Identify the blood parasite species.
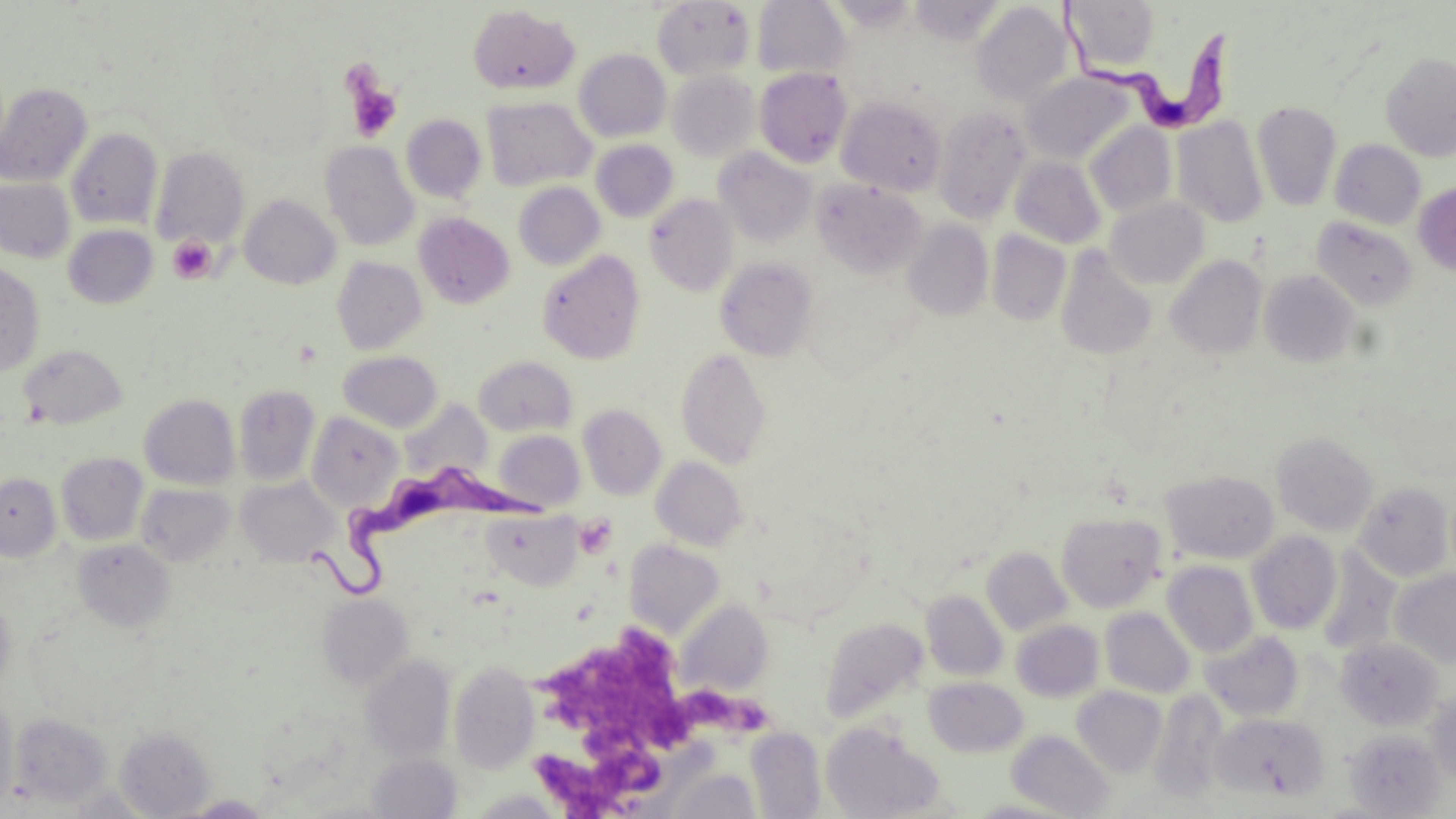
Trypanosoma brucei.

{
  "stain": "May-Grünwald-Giemsa",
  "field_of_view": "one of a larger specimen",
  "preparation": "thin blood film",
  "uninfected_red_blood_cell_locations": "approximate bounding boxes as (x1, y1, x2, y2) in pixels: (753, 0, 852, 78), (1064, 1, 1163, 76), (652, 2, 755, 79), (971, 2, 1072, 106), (467, 5, 580, 96), (574, 49, 671, 142), (1381, 52, 1456, 161), (754, 68, 852, 167), (667, 69, 760, 161), (1021, 71, 1137, 163), (0, 82, 92, 187), (482, 96, 595, 191), (837, 96, 947, 196), (1253, 100, 1341, 211), (933, 105, 1032, 222), (401, 115, 486, 203), (1172, 117, 1268, 227), (1085, 122, 1177, 217), (66, 127, 162, 229), (1330, 139, 1426, 229), (320, 140, 419, 252), (591, 140, 678, 222), (150, 146, 250, 248), (714, 147, 817, 247), (1010, 156, 1105, 248), (0, 177, 74, 263), (811, 179, 928, 279), (1413, 181, 1456, 275), (513, 182, 605, 269), (240, 194, 340, 289), (645, 194, 739, 296), (1105, 197, 1209, 289), (413, 212, 514, 308), (1312, 216, 1418, 312), (903, 220, 993, 321), (63, 225, 158, 308), (986, 231, 1070, 326), (1054, 246, 1158, 361), (538, 250, 646, 364), (1166, 255, 1267, 360), (332, 256, 428, 354), (715, 258, 818, 360), (0, 264, 46, 377), (1259, 269, 1361, 368), (19, 344, 127, 429), (676, 347, 772, 468), (337, 351, 443, 432), (473, 355, 577, 436), (235, 385, 320, 486), (139, 395, 240, 490), (398, 400, 493, 483), (578, 403, 667, 500), (306, 411, 405, 511), (493, 429, 585, 511), (1272, 431, 1378, 536), (56, 452, 148, 546), (651, 456, 749, 551), (1161, 469, 1280, 564), (0, 472, 61, 561), (237, 477, 339, 567), (1355, 482, 1454, 581), (137, 484, 235, 566), (482, 510, 582, 591), (1056, 511, 1166, 613), (1247, 531, 1342, 635), (73, 539, 175, 632), (624, 540, 725, 640), (982, 547, 1072, 636), (1162, 560, 1258, 658), (1391, 568, 1456, 668), (921, 590, 1008, 681), (0, 592, 16, 697), (317, 593, 414, 690), (677, 599, 773, 697), (1100, 607, 1196, 698), (824, 618, 929, 721), (1012, 619, 1105, 702), (1200, 630, 1304, 722), (1335, 637, 1445, 730), (360, 655, 456, 762), (449, 661, 540, 775), (924, 676, 1028, 758), (1072, 686, 1167, 778), (1149, 689, 1229, 804), (1426, 689, 1456, 782), (0, 692, 18, 812), (1210, 710, 1329, 803), (8, 711, 113, 809), (821, 722, 945, 819), (746, 727, 826, 818), (116, 728, 215, 817), (1343, 729, 1447, 818), (1007, 730, 1116, 818), (367, 753, 461, 818), (664, 766, 762, 818), (468, 791, 568, 818), (181, 795, 273, 818), (963, 797, 1082, 818)",
  "trypanosoma_brucei_locations": "approximate bounding boxes as (x1, y1, x2, y2) in pixels: (1058, 7, 1245, 137), (306, 462, 560, 609)",
  "platelet_locations": "approximate bounding boxes as (x1, y1, x2, y2) in pixels: (345, 74, 402, 141), (167, 234, 218, 285), (575, 516, 616, 558), (544, 623, 685, 766), (689, 680, 768, 741), (532, 737, 664, 819)",
  "magnification": "1000x",
  "image_size": "1456×819 pixels",
  "modality": "light microscopy"
}